State which parasite is depicted.
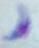
This is Toxoplasma gondii.

Summary:
  - Magnification: 1000x
  - Modality: photomicrograph